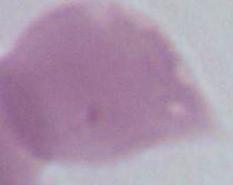 An erythrocyte is shown. Photomicrograph. 1000x magnification.